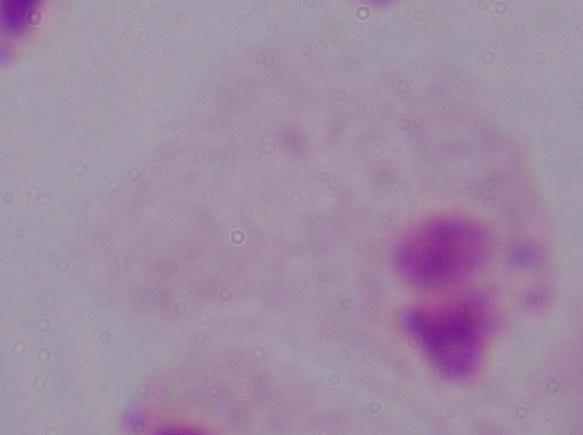

magnification = 1000x
modality = micrograph
identification = trichomonad